Assess this cell for malaria.
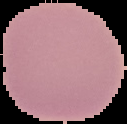

It is uninfected.

Summary:
  - Image size: 127×124 pixels
  - Preparation: thin blood smear
  - Image type: cell region segmented out of the field of view; surrounding area masked to black